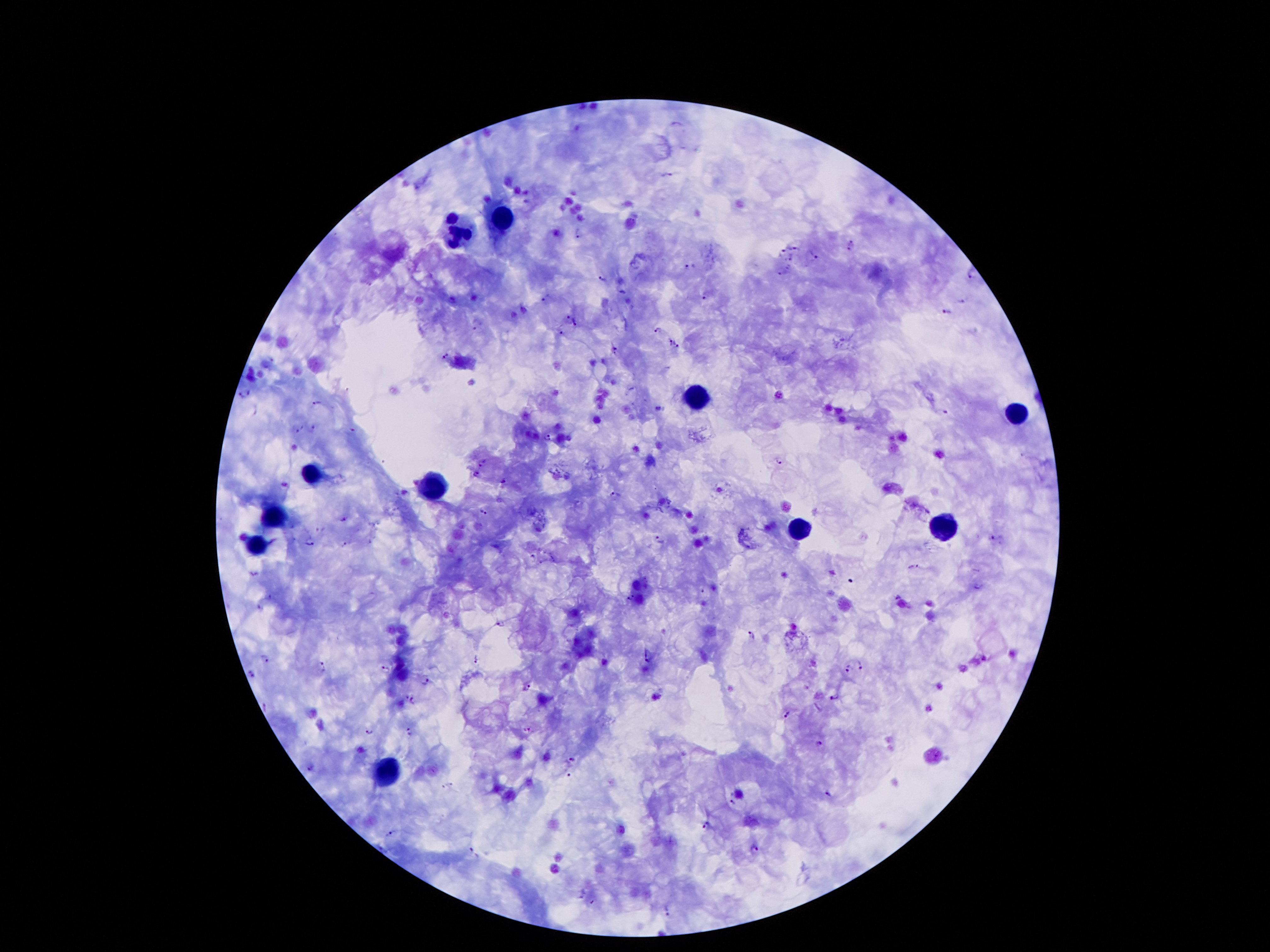
Thick peripheral-blood smear. Image is 1270×952 pixels. Giemsa-stained preparation. Single field of view. Photographed through the microscope eyepiece with a smartphone camera. Patient malaria status: infected with Plasmodium falciparum. 100x magnification.